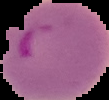

Summary:
  - Result: Plasmodium parasites detected
  - Preparation: thin blood smear
  - Image type: cell region segmented out of the field of view; surrounding area masked to black
  - Image size: 109×100 pixels